Report the malaria status of this cell.
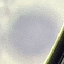
It is uninfected.

capture: smartphone through the microscope eyepiece
preparation: thin smear
stain: Giemsa
image_type: cell patch, automatically extracted from a larger field of view and resized to 64 × 64 pixels